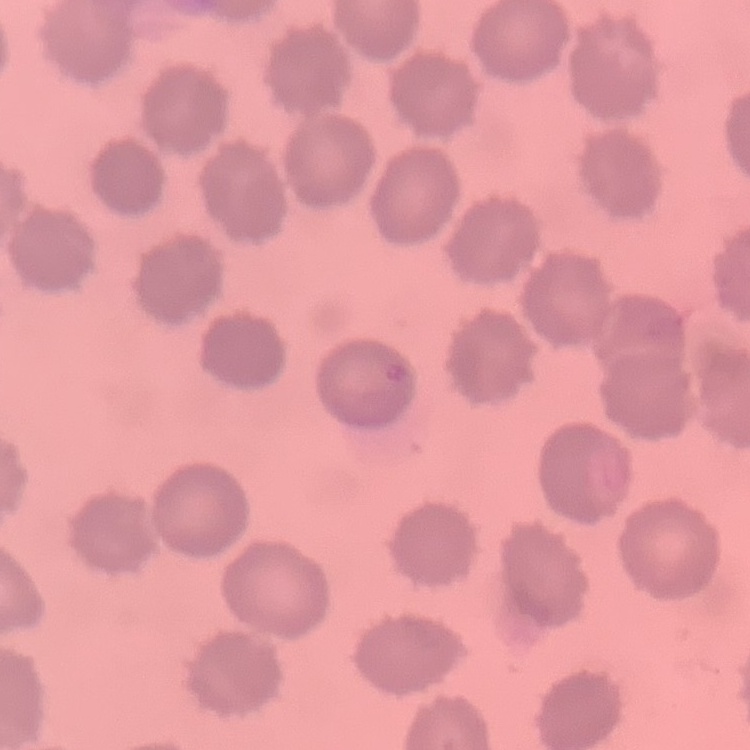

Summary:
  - Erythrocyte morphology: no rouleaux formation
  - Stain: Field's or Giemsa
  - Image type: square crop of a larger photomicrograph
  - Preparation: thin blood film